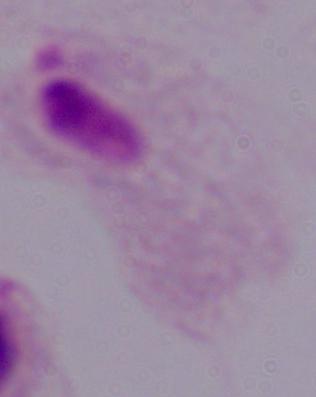
Summary:
  - Magnification: 1000x
  - Identification: trichomonad
  - Modality: photomicrograph